Assess this cell for malaria.
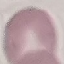
It is uninfected.

{
  "stain": "Giemsa",
  "image_type": "cell patch, automatically extracted from a larger field of view and resized to 64 × 64 pixels",
  "preparation": "thin blood smear",
  "capture": "smartphone camera at the microscope eyepiece"
}